Report the malaria status of this cell.
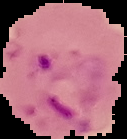

Parasitized.

The area outside the segmented cell region is set to black. From a thin blood smear. Image is 127×139 pixels.